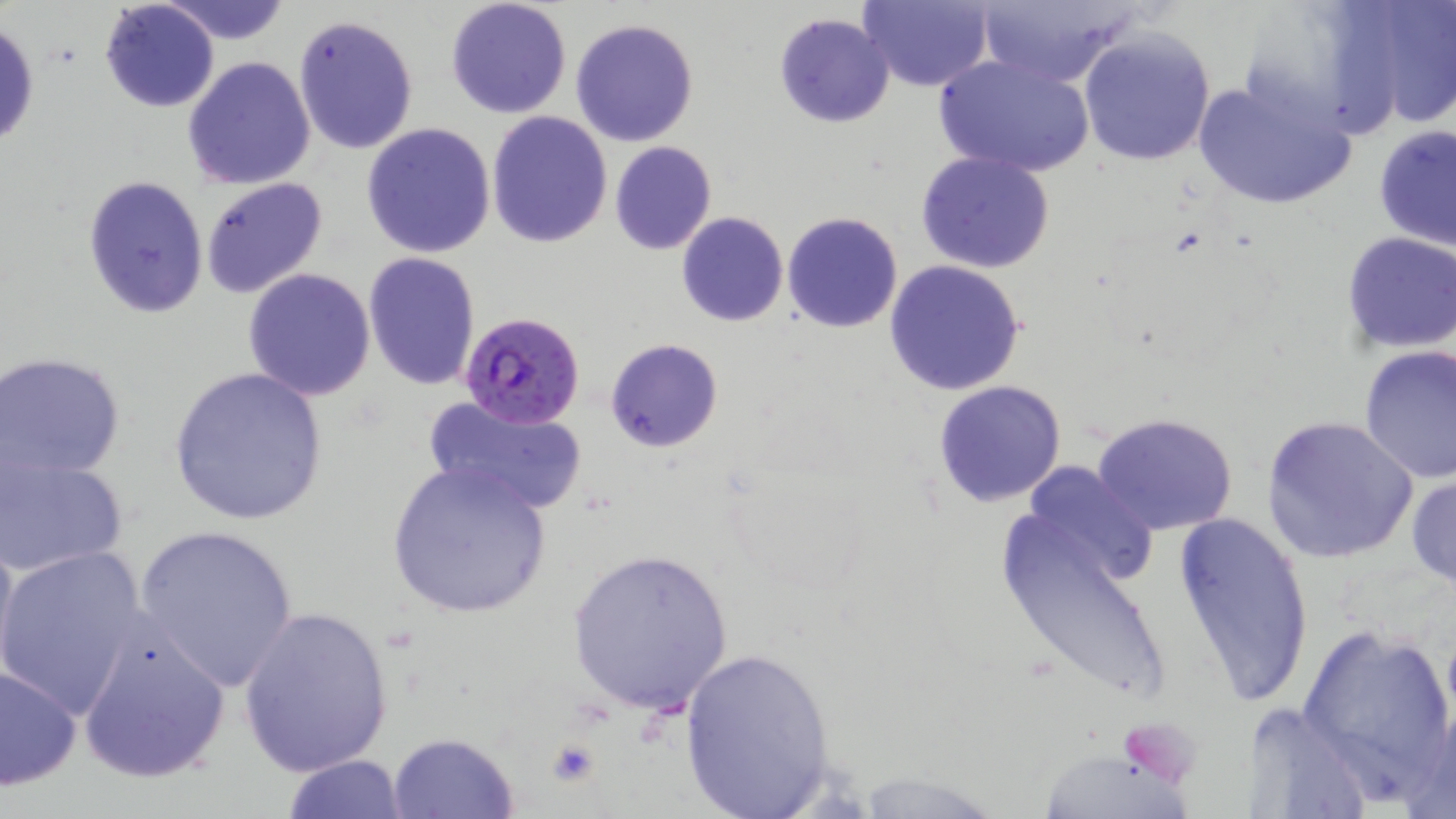
slide_level_diagnosis: Plasmodium falciparum
uninfected_red_blood_cell_locations: 'approximate bounding boxes as (x1, y1, x2, y2) in pixels: (99, 0, 219, 113), (444, 0, 573, 120), (856, 0, 995, 91), (1344, 0, 1456, 131), (161, 1, 293, 46), (972, 2, 1135, 86), (773, 13, 893, 128), (293, 14, 420, 156), (1, 18, 41, 152), (570, 18, 698, 147), (1079, 29, 1215, 165), (932, 51, 1096, 177), (181, 57, 316, 191), (1191, 76, 1357, 212), (486, 111, 614, 249), (360, 122, 496, 258), (1373, 124, 1455, 252), (609, 141, 717, 255), (915, 151, 1055, 273), (81, 174, 210, 319), (201, 178, 328, 299), (677, 211, 789, 327), (782, 211, 904, 333), (1340, 232, 1456, 352), (362, 252, 482, 391), (883, 260, 1027, 397), (242, 269, 376, 401), (605, 338, 724, 452), (1358, 347, 1456, 484), (1, 352, 127, 482), (165, 367, 330, 527), (932, 380, 1066, 507), (423, 392, 588, 516), (1092, 412, 1241, 537), (1260, 415, 1418, 563), (0, 445, 128, 580), (383, 459, 555, 619), (1017, 461, 1158, 586), (1407, 473, 1456, 590), (996, 499, 1172, 710), (1172, 510, 1314, 707), (0, 521, 19, 683), (132, 523, 301, 692), (0, 546, 149, 725), (566, 547, 733, 717), (237, 604, 396, 778), (72, 618, 234, 785), (1294, 622, 1456, 796), (675, 644, 840, 819), (0, 663, 81, 791), (1247, 700, 1376, 819), (388, 732, 518, 817), (1035, 742, 1197, 817), (281, 753, 409, 819)'
modality: light microscopy
plasmodium_falciparum_infected_red_blood_cell_locations: 'approximate bounding boxes as (x1, y1, x2, y2) in pixels: (459, 311, 585, 428)'
field_of_view: one of a larger specimen
magnification: 1000x
image_size: 1456×819 pixels
stain: May-Grünwald-Giemsa
preparation: thin blood film
platelet_locations: 'approximate bounding boxes as (x1, y1, x2, y2) in pixels: (544, 739, 600, 787)'